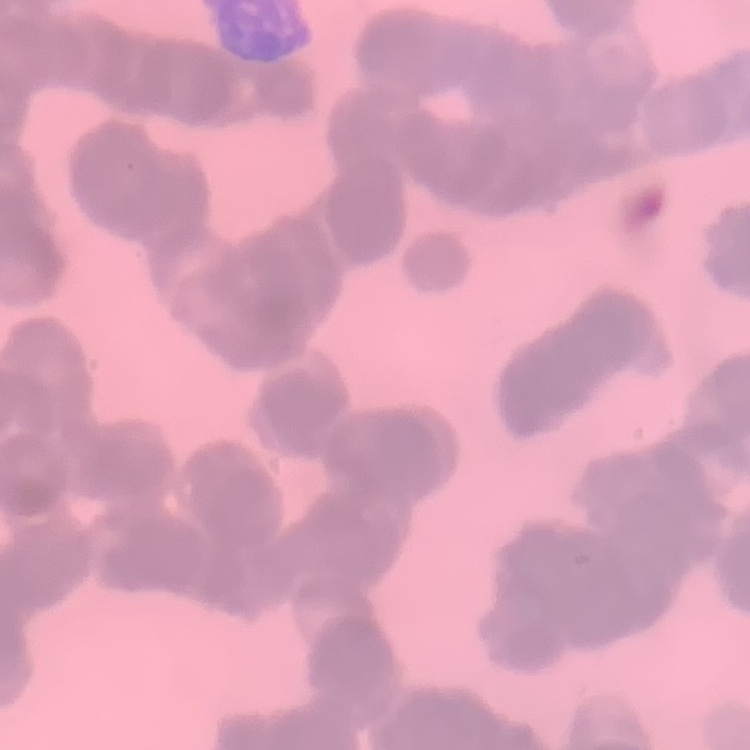

The red blood cells exhibit rouleaux formation. Thin peripheral smear. Field's or Giemsa stain. Square crop of a larger photomicrograph.